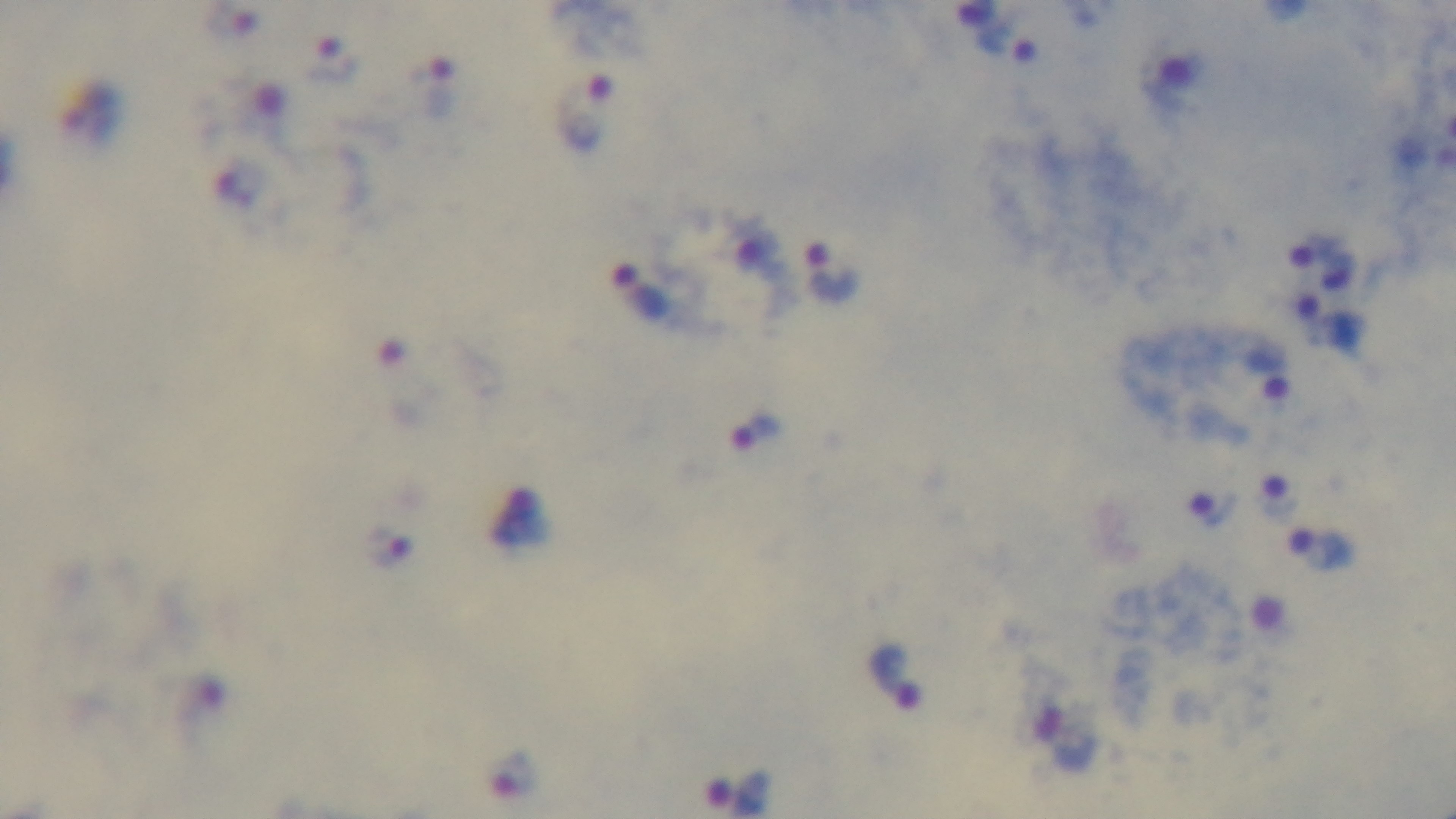

capture = mounted 4K digital camera
objective = 100x oil immersion
preparation = thick
modality = light microscopy
stain = Giemsa
malaria status = infected
field of view = single